State which parasite is depicted.
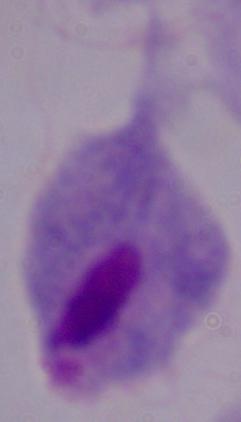

This is a trichomonad.

Summary:
  - Magnification: 1000x
  - Modality: photomicrograph